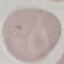

Summary:
  - Result: negative for malaria parasites
  - Stain: Giemsa
  - Preparation: thin smear
  - Capture: smartphone through the microscope eyepiece
  - Image type: automatically extracted cell patch, resized to 64 × 64 pixels